Outline each blood parasite and name the species.
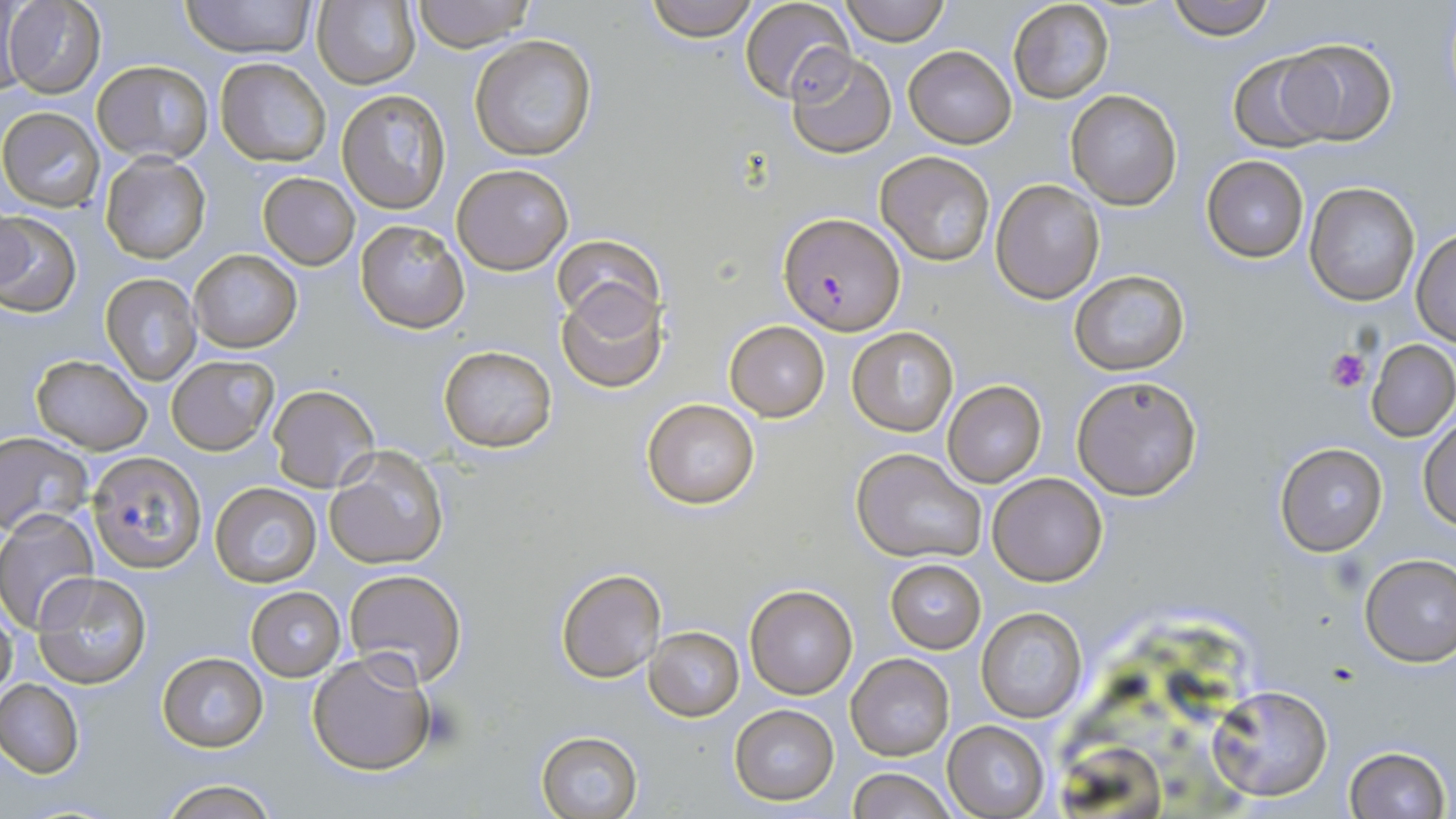
Approximate bounding boxes as [x1, y1, x2, y2] in pixels.
Plasmodium falciparum-infected red blood cells: [780, 211, 904, 335].
No Plasmodium ovale, Plasmodium malariae, Plasmodium vivax, Babesia divergens, or Trypanosoma brucei observed.

{
  "slide_level_diagnosis": "Plasmodium falciparum",
  "image_size": "1456×819 pixels",
  "field_of_view": "one of a larger specimen",
  "uninfected_red_blood_cell_locations": "approximate bounding boxes as [x1, y1, x2, y2] in pixels: [179, 0, 316, 59], [410, 0, 536, 52], [643, 0, 761, 42], [739, 0, 855, 105], [840, 0, 949, 45], [1008, 0, 1115, 104], [1166, 0, 1275, 40], [2, 1, 105, 98], [314, 1, 423, 91], [0, 4, 25, 102], [469, 34, 597, 162], [1278, 36, 1398, 145], [903, 46, 1017, 147], [785, 50, 899, 159], [1228, 56, 1333, 152], [215, 58, 332, 167], [92, 60, 214, 164], [1064, 89, 1182, 210], [337, 90, 448, 213], [1, 107, 104, 213], [876, 151, 998, 265], [99, 153, 213, 262], [1202, 155, 1309, 262], [451, 163, 574, 275], [258, 172, 360, 270], [991, 179, 1106, 303], [1304, 181, 1421, 306], [0, 212, 81, 316], [356, 219, 469, 333], [1411, 229, 1456, 346], [552, 236, 665, 331], [188, 248, 303, 353], [1069, 270, 1190, 376], [101, 273, 200, 383], [556, 283, 667, 392], [725, 321, 830, 420], [847, 326, 959, 437], [1365, 337, 1456, 442], [438, 345, 558, 452], [29, 355, 153, 454], [166, 355, 279, 456], [1073, 376, 1203, 501], [942, 380, 1047, 486], [267, 384, 380, 493], [641, 397, 762, 511], [1419, 415, 1456, 531], [0, 433, 93, 536], [1275, 442, 1388, 555], [324, 448, 450, 570], [851, 448, 987, 564], [89, 452, 208, 574], [988, 472, 1109, 587], [209, 481, 322, 587], [0, 510, 99, 631], [1358, 553, 1456, 667], [885, 559, 986, 652], [555, 566, 667, 684], [343, 569, 466, 686], [33, 571, 152, 688], [744, 584, 858, 698], [246, 586, 345, 681], [975, 608, 1088, 724], [0, 611, 17, 706], [645, 626, 744, 720], [306, 648, 437, 778], [156, 652, 269, 751], [847, 654, 954, 761], [0, 679, 84, 777], [1207, 683, 1335, 804], [730, 705, 839, 805], [943, 721, 1049, 817], [535, 730, 644, 819], [1058, 745, 1174, 818], [1341, 746, 1450, 819], [845, 765, 956, 819], [156, 779, 280, 819]",
  "platelet_locations": "approximate bounding boxes as [x1, y1, x2, y2] in pixels: [1328, 348, 1370, 393]",
  "magnification": "1000x",
  "stain": "May-Grünwald-Giemsa",
  "modality": "light microscopy",
  "preparation": "thin blood smear"
}